Report the malaria status of this cell.
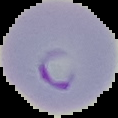
Parasitized.

Summary:
  - Image size: 118×118 pixels
  - Preparation: thin blood smear
  - Image type: segmented cell region on a black background